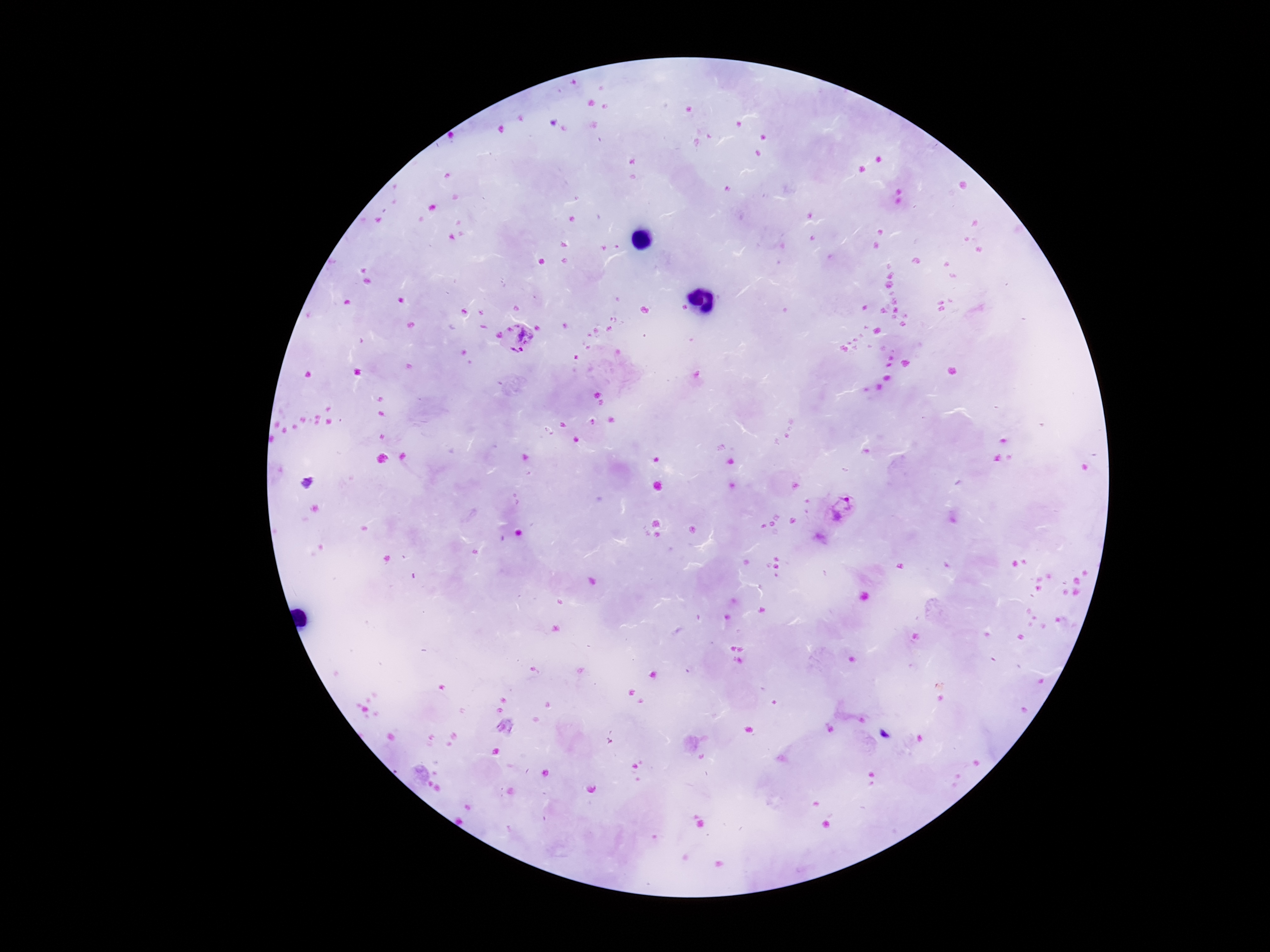
preparation = thick blood smear
image size = 1270×952 pixels
field of view = single
patient malaria status = positive
capture = smartphone camera through the microscope eyepiece
magnification = 100x
stain = Giemsa
Plasmodium parasite locations = approximate object centers, in pixels from the top-left corner: (x=525, y=337), (x=515, y=355), (x=841, y=509)